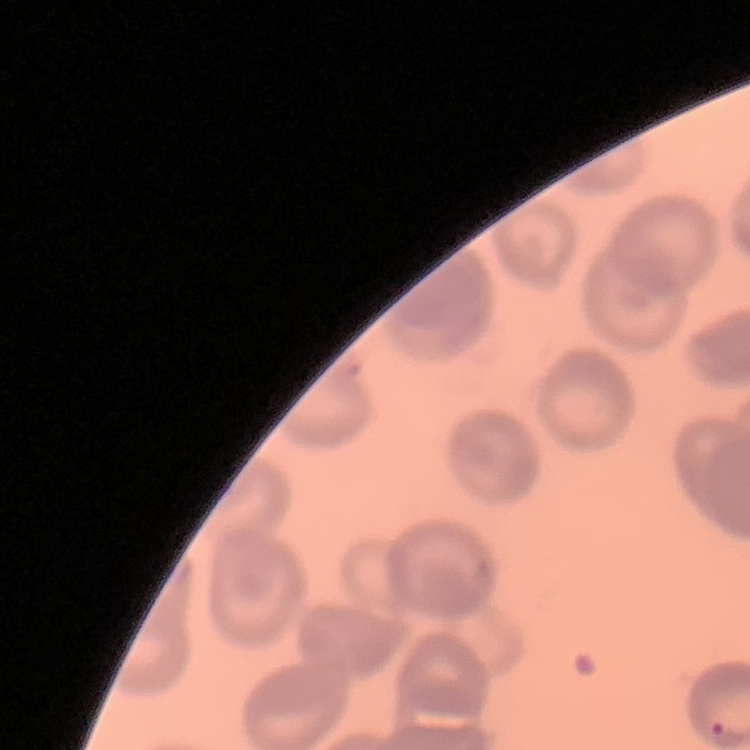

The erythrocytes exhibit no rouleaux formation. Thin blood film. Stained with either Field's or Giemsa. One tile cut from a larger photomicrograph.